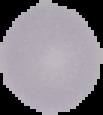

Cell region segmented out of the field of view; the surrounding area is masked to black. Malaria status: uninfected. From a thin blood film. Image is 103×115 pixels.